Name the blood parasite species.
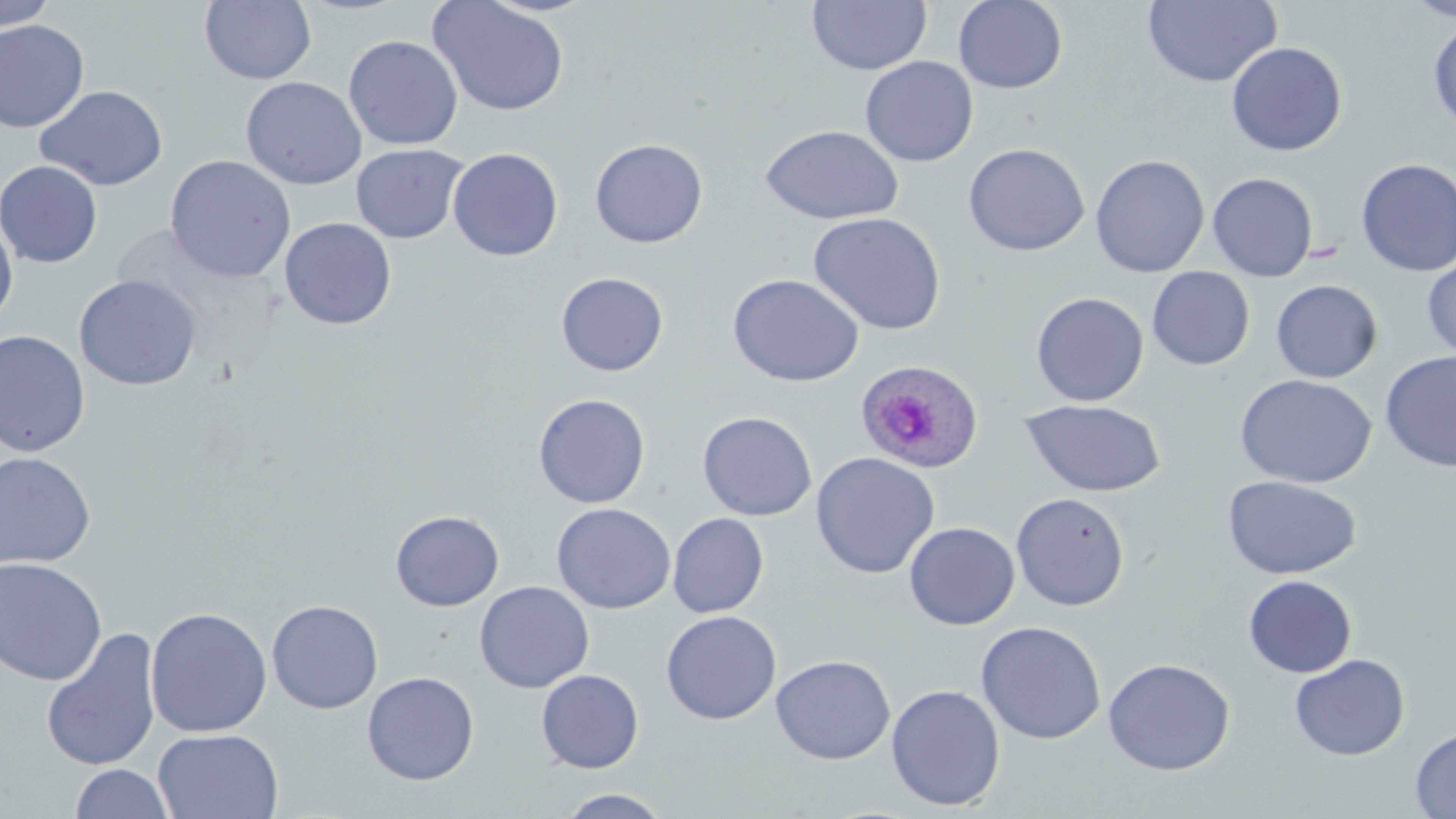
Plasmodium ovale.

image size = 1456×819 pixels
stain = May-Grünwald-Giemsa
preparation = thin blood film
Plasmodium ovale-infected red blood cell locations = approximate bounding boxes as [x1, y1, x2, y2] in pixels: [857, 356, 986, 475]
magnification = 1000x
field of view = single
uninfected red blood cell locations = approximate bounding boxes as [x1, y1, x2, y2] in pixels: [0, 0, 58, 32], [953, 0, 1068, 94], [1143, 0, 1282, 87], [1405, 0, 1456, 22], [199, 1, 317, 85], [428, 1, 569, 117], [807, 1, 932, 75], [1429, 17, 1456, 131], [0, 20, 90, 133], [344, 35, 463, 150], [1226, 42, 1347, 156], [860, 56, 978, 167], [241, 77, 367, 190], [35, 85, 168, 190], [759, 125, 904, 224], [589, 138, 708, 248], [963, 142, 1090, 256], [351, 144, 468, 244], [448, 148, 563, 262], [1090, 154, 1210, 278], [165, 155, 296, 283], [1355, 158, 1456, 277], [0, 160, 103, 267], [1207, 172, 1318, 282], [808, 212, 947, 335], [279, 217, 397, 330], [0, 218, 18, 325], [1422, 254, 1456, 362], [1147, 267, 1255, 370], [555, 272, 669, 376], [727, 273, 864, 387], [74, 275, 201, 391], [1271, 280, 1383, 383], [1031, 292, 1149, 407], [0, 330, 90, 457], [1379, 351, 1456, 471], [1236, 374, 1376, 488], [532, 393, 651, 508], [1021, 400, 1166, 497], [697, 411, 817, 521], [0, 452, 96, 571], [810, 452, 940, 579], [1222, 475, 1362, 579], [1011, 492, 1130, 611], [552, 503, 676, 614], [390, 509, 504, 611], [668, 513, 769, 618], [903, 522, 1020, 630], [0, 557, 107, 686], [1243, 575, 1357, 678], [474, 581, 595, 693], [267, 600, 383, 714], [145, 607, 272, 738], [661, 610, 781, 724], [975, 621, 1105, 745], [41, 629, 162, 772], [1290, 653, 1410, 761], [770, 655, 895, 765], [1102, 658, 1235, 775], [536, 669, 644, 774], [362, 671, 480, 785], [886, 684, 1005, 811], [1410, 727, 1456, 818], [153, 728, 283, 819], [69, 763, 174, 819], [556, 788, 674, 818]
modality = light microscopy